Assess this cell for malaria.
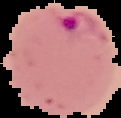

It is parasitized.

preparation = thin blood smear
image type = segmented cell region with the area outside set to black
image size = 121×118 pixels